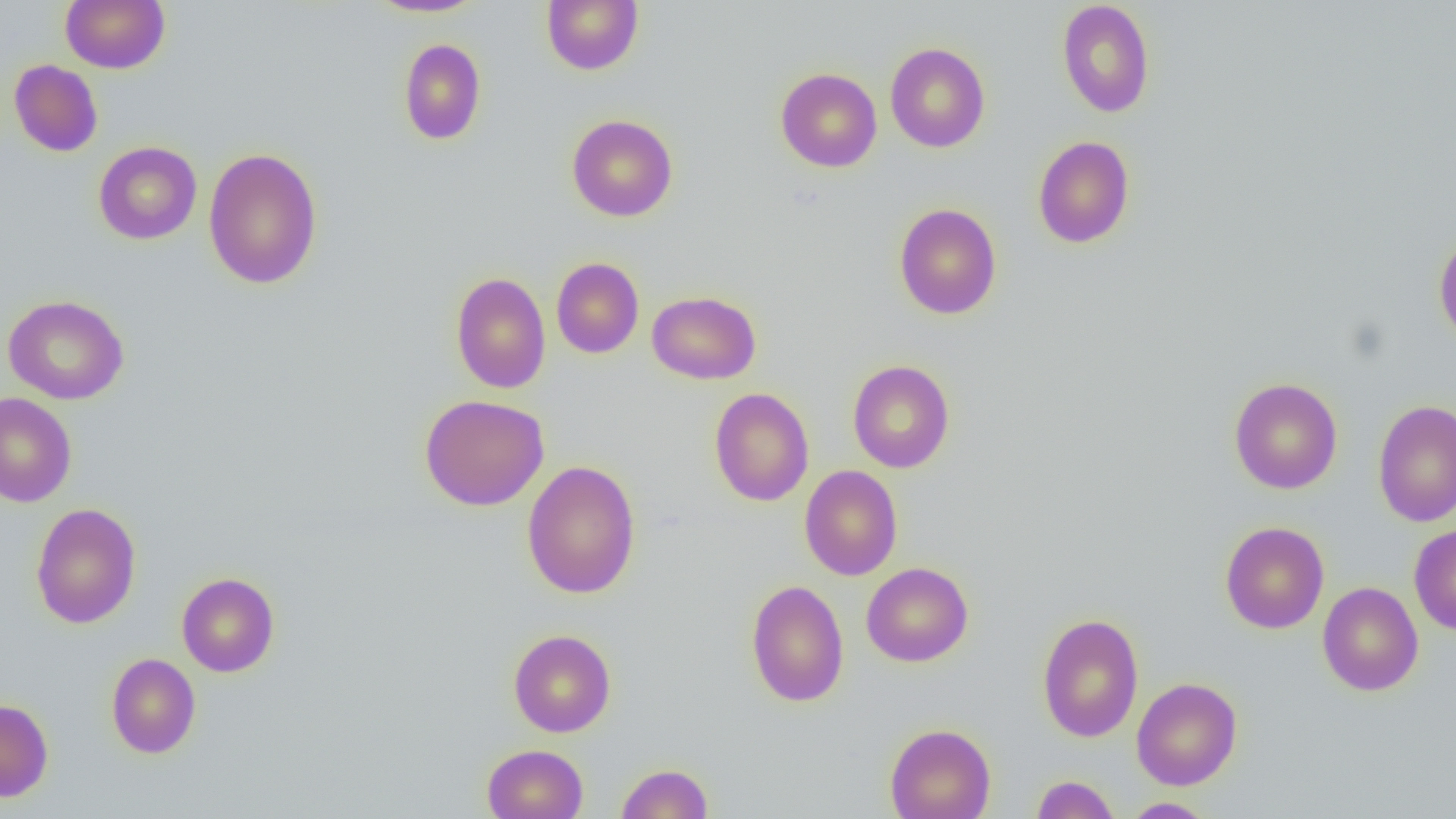

Summary:
  - Coordinate format: approximate bounding boxes as named x1/y1/x2/y2 corners in pixels
  - Uninfected red blood cell locations: (x1=60, y1=0, x2=170, y2=73), (x1=366, y1=0, x2=488, y2=18), (x1=541, y1=0, x2=643, y2=74), (x1=1057, y1=1, x2=1155, y2=118), (x1=398, y1=38, x2=487, y2=145), (x1=885, y1=42, x2=990, y2=152), (x1=9, y1=59, x2=103, y2=157), (x1=775, y1=68, x2=882, y2=172), (x1=567, y1=114, x2=678, y2=222), (x1=1033, y1=136, x2=1135, y2=248), (x1=93, y1=141, x2=202, y2=245), (x1=203, y1=147, x2=323, y2=289), (x1=894, y1=203, x2=1002, y2=319), (x1=1433, y1=232, x2=1456, y2=348), (x1=551, y1=257, x2=644, y2=358), (x1=451, y1=264, x2=645, y2=368), (x1=450, y1=271, x2=551, y2=393), (x1=647, y1=291, x2=761, y2=384), (x1=3, y1=294, x2=130, y2=405), (x1=847, y1=360, x2=955, y2=473), (x1=1229, y1=377, x2=1343, y2=494), (x1=709, y1=388, x2=814, y2=506), (x1=0, y1=393, x2=77, y2=507), (x1=419, y1=394, x2=550, y2=512), (x1=1373, y1=399, x2=1456, y2=527), (x1=521, y1=460, x2=641, y2=599), (x1=799, y1=465, x2=902, y2=581), (x1=30, y1=503, x2=141, y2=629), (x1=1219, y1=521, x2=1329, y2=634), (x1=1408, y1=524, x2=1456, y2=635), (x1=861, y1=562, x2=974, y2=667), (x1=176, y1=572, x2=280, y2=677), (x1=746, y1=579, x2=849, y2=707), (x1=1317, y1=581, x2=1424, y2=696), (x1=1036, y1=612, x2=1144, y2=743), (x1=508, y1=629, x2=616, y2=737), (x1=106, y1=653, x2=201, y2=758), (x1=1131, y1=677, x2=1243, y2=790), (x1=0, y1=698, x2=54, y2=802), (x1=884, y1=723, x2=995, y2=819), (x1=482, y1=743, x2=588, y2=819), (x1=616, y1=763, x2=713, y2=818), (x1=1030, y1=775, x2=1120, y2=819), (x1=1120, y1=797, x2=1217, y2=818)
  - Slide-level diagnosis: negative for blood parasites
  - Preparation: thin blood smear
  - Field of view: one of a larger specimen
  - Image size: 1456×819 pixels
  - Modality: optical microscopy
  - Magnification: 1000x